Outline each blood parasite and name the species.
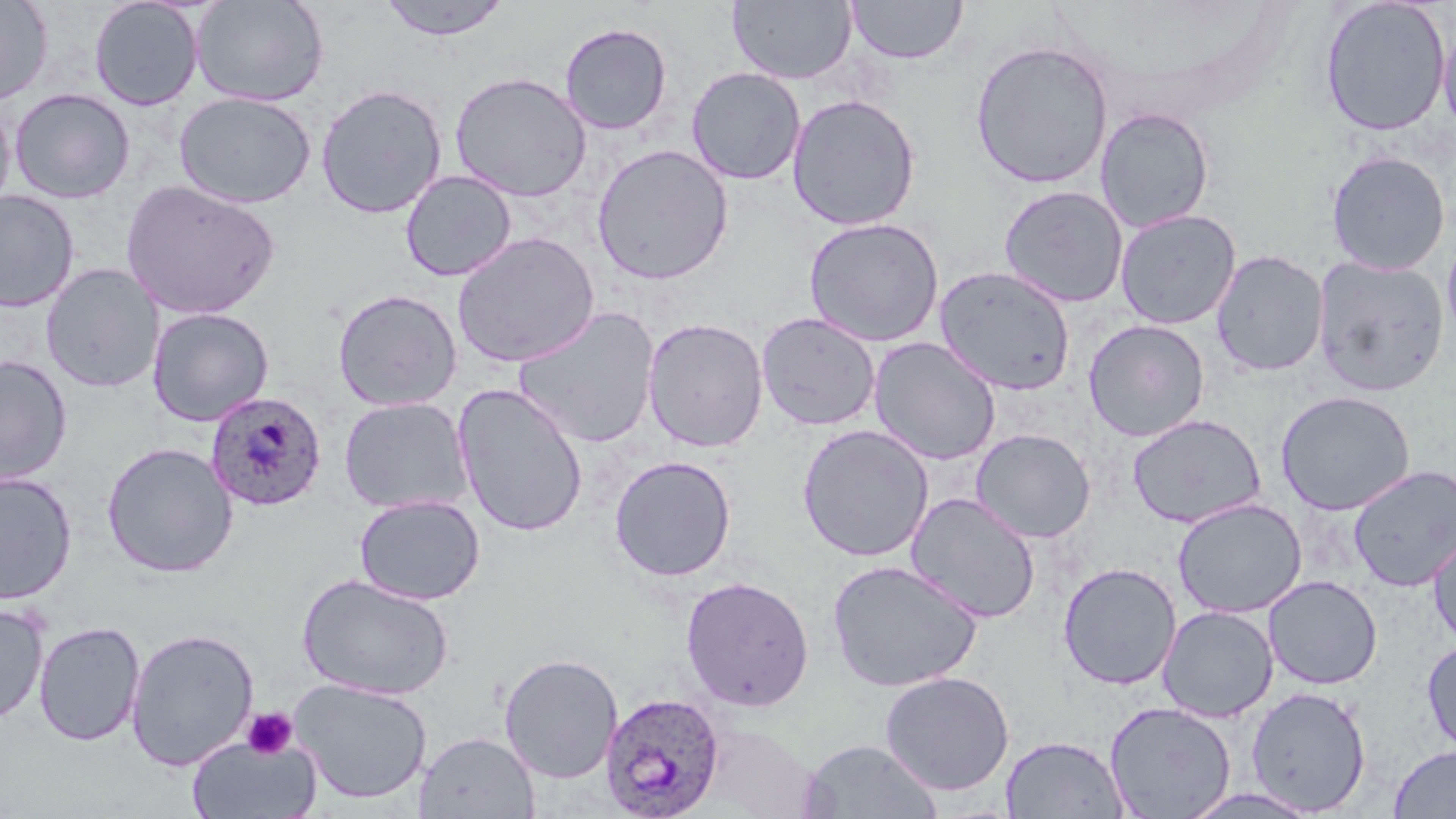
Approximate bounding boxes as (x1, y1, x2, y2) in pixels.
Plasmodium ovale-infected red blood cells: (204, 390, 327, 511), (599, 691, 726, 818).
No Plasmodium falciparum, Plasmodium malariae, Plasmodium vivax, Babesia divergens, or Trypanosoma brucei observed.

Platelet locations: (242, 708, 299, 760). Uninfected red blood cell locations: (0, 0, 53, 106), (88, 0, 204, 111), (191, 0, 329, 107), (377, 0, 513, 42), (846, 0, 968, 64), (1318, 0, 1450, 137), (728, 1, 857, 85), (1438, 17, 1455, 141), (560, 22, 672, 135), (969, 40, 1114, 189), (686, 66, 806, 185), (450, 71, 592, 202), (315, 84, 448, 219), (9, 88, 135, 204), (174, 92, 316, 208), (786, 93, 921, 231), (0, 96, 16, 221), (1095, 106, 1215, 233), (591, 143, 733, 285), (1325, 150, 1451, 275), (400, 170, 517, 282), (121, 180, 281, 320), (998, 185, 1129, 308), (0, 190, 79, 312), (1114, 208, 1242, 329), (803, 217, 944, 347), (1441, 230, 1456, 350), (452, 232, 600, 368), (1211, 249, 1329, 377), (1313, 254, 1450, 397), (41, 263, 163, 393), (934, 264, 1076, 396), (331, 289, 463, 411), (512, 305, 661, 449), (147, 307, 274, 427), (756, 312, 880, 431), (642, 317, 769, 453), (1083, 319, 1211, 442), (867, 336, 1001, 466), (0, 355, 73, 487), (452, 382, 589, 538), (1275, 390, 1416, 516), (338, 397, 474, 515), (1126, 414, 1266, 528), (797, 423, 934, 562), (970, 428, 1096, 543), (101, 442, 238, 577), (608, 455, 737, 582), (1348, 465, 1456, 592), (0, 471, 77, 605), (905, 491, 1041, 623), (354, 494, 485, 605), (1172, 498, 1307, 618), (1428, 526, 1456, 651), (826, 559, 983, 692), (1058, 563, 1181, 690), (296, 573, 455, 701), (680, 575, 814, 711), (1263, 575, 1383, 689), (0, 601, 49, 724), (1158, 606, 1279, 722), (33, 621, 145, 747), (126, 627, 259, 771), (1422, 637, 1456, 759), (499, 653, 623, 784), (878, 671, 1015, 795), (290, 677, 432, 804), (1246, 686, 1371, 814), (1104, 701, 1236, 818), (414, 731, 540, 819), (187, 735, 322, 818), (1000, 735, 1129, 818), (799, 739, 943, 819), (1388, 746, 1456, 818), (1179, 788, 1321, 818). Slide-level diagnosis: Plasmodium ovale. Thin blood film. 1000x magnification. May-Grünwald-Giemsa-stained preparation. Optical microscopy. One field of a larger specimen. Image is 1456×819 pixels.